Assess this cell for malaria.
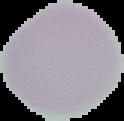

It is uninfected.

{
  "image_type": "cell region segmented out of the field of view; surrounding area masked to black",
  "image_size": "124×121 pixels",
  "preparation": "thin blood film"
}